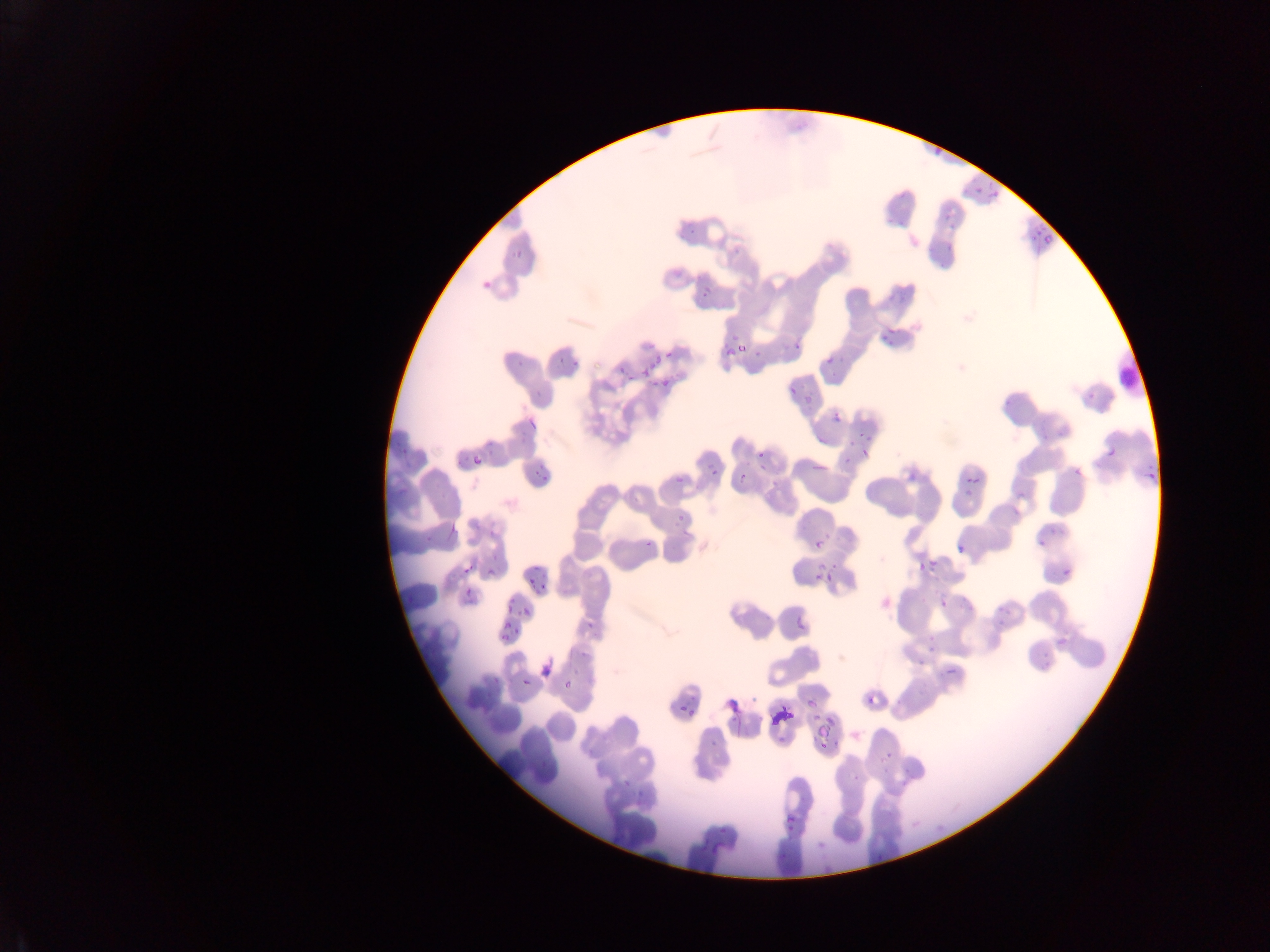
image size = 1270×952 pixels
malaria parasite locations = approximate bounding boxes as (left, top, right, bottom) in pixels: (976, 173, 1004, 205), (1032, 221, 1053, 251), (512, 250, 528, 261), (479, 277, 495, 294), (702, 284, 711, 298), (872, 332, 903, 352), (550, 341, 586, 371), (718, 343, 749, 360), (783, 343, 799, 356), (821, 351, 851, 372), (643, 354, 660, 376), (612, 358, 632, 376), (656, 374, 676, 393), (794, 388, 812, 406), (1078, 388, 1099, 398), (770, 396, 797, 408), (523, 408, 547, 434), (831, 411, 845, 425), (470, 438, 498, 471), (854, 441, 880, 458), (1102, 442, 1122, 464), (533, 453, 555, 487), (730, 456, 760, 497), (1069, 456, 1088, 479), (704, 459, 720, 477), (1140, 468, 1162, 486), (962, 471, 984, 500), (440, 501, 466, 545), (665, 503, 684, 536), (487, 525, 501, 541), (1031, 526, 1041, 555), (642, 536, 657, 554), (953, 538, 973, 559), (805, 539, 825, 550), (1057, 552, 1081, 574), (908, 559, 934, 582), (481, 564, 495, 580), (805, 569, 839, 585), (523, 573, 546, 596), (458, 580, 477, 608), (927, 584, 963, 611), (520, 605, 533, 619), (796, 620, 809, 634), (499, 621, 512, 641), (538, 659, 554, 689), (941, 663, 961, 683), (520, 676, 534, 690), (562, 677, 575, 692), (727, 690, 738, 714), (864, 690, 883, 711), (674, 702, 686, 716), (764, 704, 797, 728), (808, 710, 835, 742), (782, 811, 799, 838), (705, 818, 732, 859)
capture = mobile-phone photograph through a microscope
country = Ghana
field of view = single
preparation = thin blood film